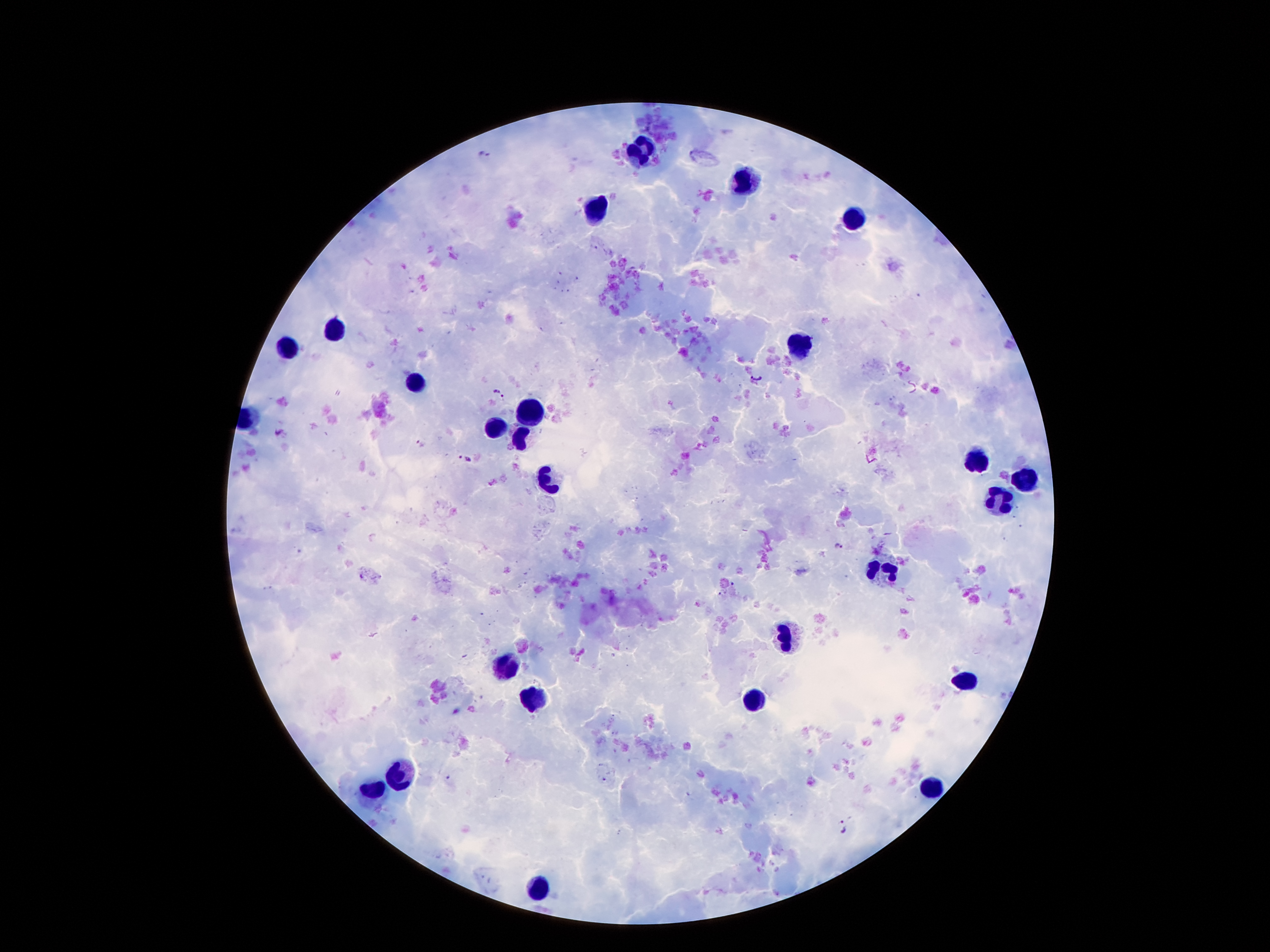

Approximate centers as (x, y) in pixels. Malaria parasite locations: (486, 154), (757, 379), (501, 393), (422, 445), (467, 458), (838, 546), (723, 594), (845, 825). Leukocyte locations: (639, 149), (741, 181), (596, 212), (857, 220), (338, 330), (287, 345), (797, 347), (415, 384), (534, 415), (498, 429), (521, 439), (975, 460), (1023, 477), (549, 481), (992, 498), (883, 571), (784, 636), (504, 667), (964, 678), (534, 698), (755, 702), (397, 775), (929, 788), (372, 790), (537, 892). 100x magnification. Patient malaria status: positive for Plasmodium falciparum. Thick peripheral-blood smear. Single field of view. Photographed through the microscope eyepiece with a smartphone camera. Giemsa stain. Image is 1270×952 pixels.